State the preparation type.
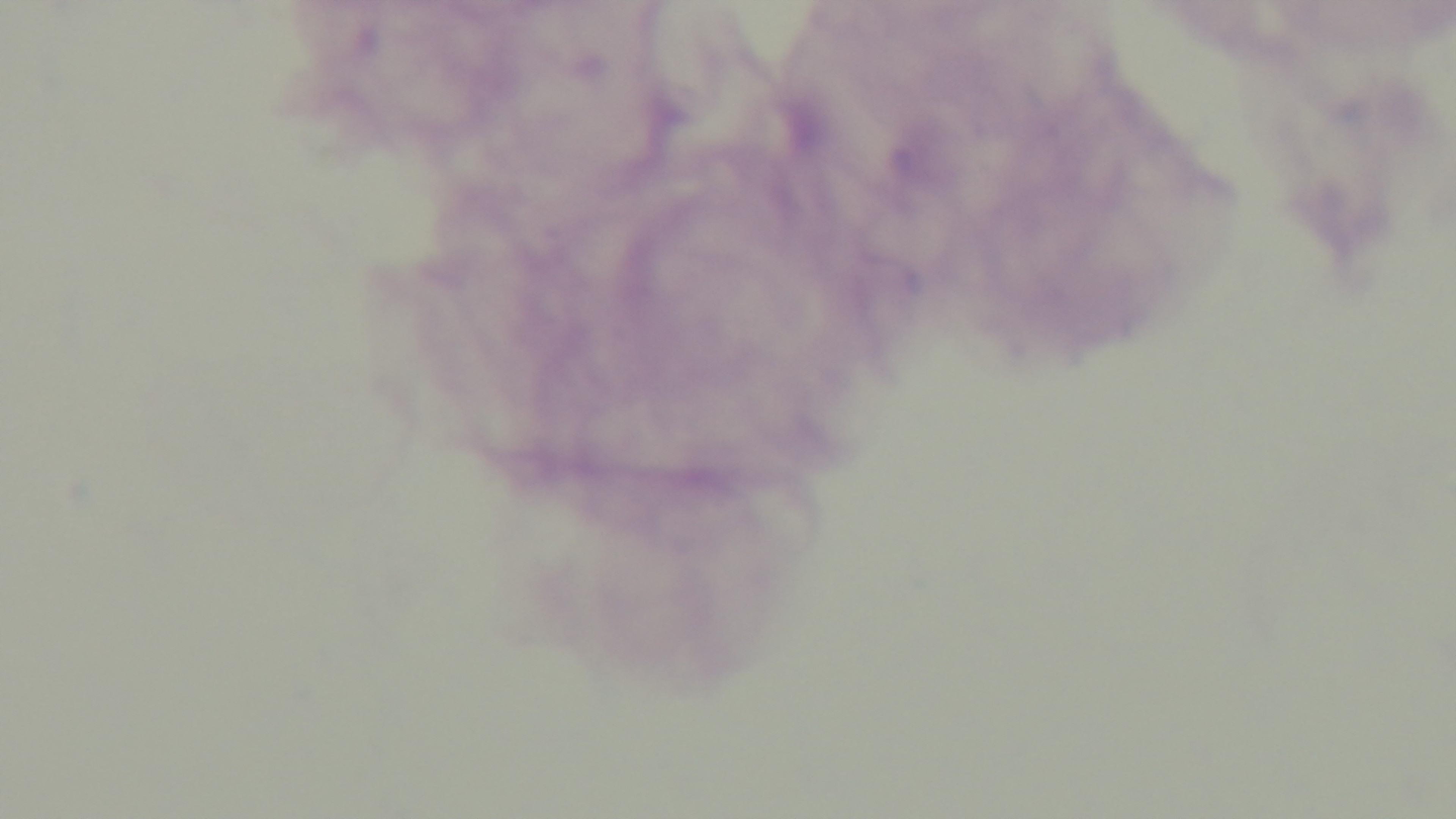

Thick.

Mounted 4K digital camera. Giemsa-stained. Oil-immersion objective, 100x. Single field of view. Photomicrograph. Malaria status: uninfected.